Locate every blood parasite and identify its species.
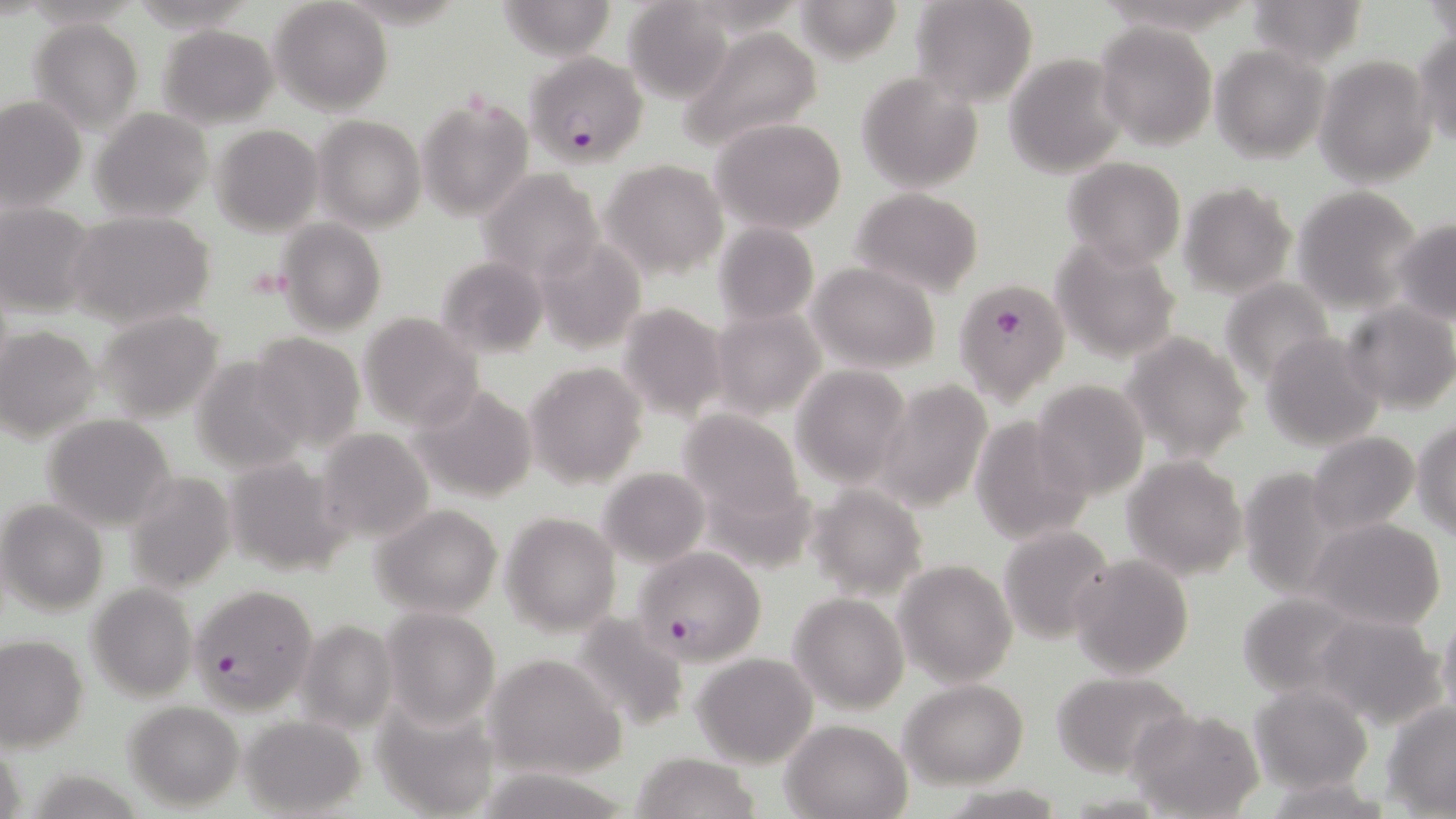

Approximate bounding boxes as [x1, y1, x2, y2] in pixels.
Plasmodium falciparum-infected red blood cells: [531, 54, 650, 176], [952, 280, 1068, 402], [634, 546, 767, 666], [187, 582, 318, 716].
No Plasmodium ovale, Plasmodium malariae, Plasmodium vivax, Babesia divergens, or Trypanosoma brucei observed.

Platelet locations: [244, 265, 293, 300]. Uninfected red blood cell locations: [792, 0, 907, 64], [910, 0, 1038, 107], [1243, 0, 1369, 68], [270, 1, 392, 116], [496, 1, 619, 60], [623, 1, 735, 105], [1424, 2, 1455, 48], [27, 17, 144, 132], [1094, 22, 1217, 150], [156, 24, 279, 129], [678, 24, 824, 154], [1411, 31, 1456, 148], [1210, 46, 1330, 163], [1003, 53, 1128, 177], [1314, 54, 1438, 187], [857, 71, 984, 192], [416, 94, 533, 221], [0, 95, 86, 212], [91, 108, 213, 223], [314, 116, 425, 232], [711, 117, 847, 235], [211, 123, 323, 234], [1061, 157, 1187, 271], [602, 159, 728, 278], [478, 168, 604, 285], [1179, 182, 1298, 299], [1291, 185, 1423, 313], [851, 186, 984, 297], [0, 204, 98, 318], [64, 210, 215, 330], [1393, 217, 1456, 323], [277, 218, 386, 336], [713, 222, 818, 326], [533, 236, 647, 353], [1050, 237, 1182, 363], [435, 256, 550, 359], [807, 262, 941, 374], [1219, 278, 1337, 386], [1343, 301, 1456, 415], [617, 302, 730, 420], [710, 307, 825, 421], [95, 310, 224, 424], [358, 313, 484, 430], [0, 325, 104, 442], [248, 331, 365, 451], [1121, 331, 1254, 463], [1259, 331, 1385, 451], [190, 354, 311, 476], [525, 362, 649, 488], [791, 365, 911, 487], [874, 379, 992, 512], [1031, 380, 1149, 499], [410, 383, 540, 505], [678, 409, 805, 521], [969, 412, 1093, 543], [41, 413, 177, 532], [1413, 420, 1456, 539], [316, 429, 434, 542], [1304, 432, 1422, 538], [219, 452, 350, 578], [1122, 455, 1248, 580], [598, 466, 710, 567], [122, 472, 235, 594], [1247, 474, 1397, 617], [806, 485, 928, 600], [1, 500, 107, 614], [372, 503, 505, 618], [502, 511, 620, 636], [1306, 519, 1445, 632], [997, 524, 1117, 646], [1068, 554, 1194, 679], [894, 560, 1016, 686], [86, 582, 197, 702], [1234, 591, 1368, 696], [790, 592, 908, 713], [381, 607, 500, 729], [1436, 609, 1456, 732], [1310, 613, 1446, 729], [567, 614, 689, 732], [298, 619, 398, 734], [0, 635, 88, 751], [484, 652, 626, 779], [692, 653, 817, 767], [1051, 671, 1191, 777], [901, 679, 1028, 787], [1249, 685, 1373, 792], [371, 695, 502, 819], [1383, 700, 1456, 815], [123, 701, 245, 812], [1129, 708, 1264, 819], [240, 712, 366, 817], [781, 718, 914, 818], [631, 753, 760, 819], [1265, 776, 1395, 817], [945, 784, 1069, 817]. Slide-level diagnosis: Plasmodium falciparum. Thin blood smear. Optical microscopy. Image is 1456×819 pixels. Captured at 1000x magnification. May-Grünwald-Giemsa stain. One field of a larger specimen.